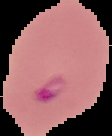
malaria status = parasitized
image type = segmented cell region with the area outside set to black
image size = 112×136 pixels
preparation = thin blood film